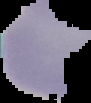

From a thin blood smear. Image is 91×103 pixels. Malaria status: uninfected. The area outside the segmented cell region is set to black.